Classify this cell by malaria status.
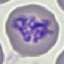

It is parasitized.

preparation = thin smear
capture = smartphone through the microscope eyepiece
stain = Giemsa
image type = automatically extracted cell patch, resized to 64 × 64 pixels